Assess this cell for malaria.
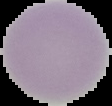
Uninfected.

From a thin blood film. Image is 112×106 pixels. Segmented cell region on a black background.